Report the malaria status of this cell.
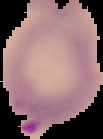

Parasitized.

Summary:
  - Image size: 103×139 pixels
  - Image type: cell region segmented out of the field of view; surrounding area masked to black
  - Preparation: thin blood film